Comment on the morphology of the red blood cells.
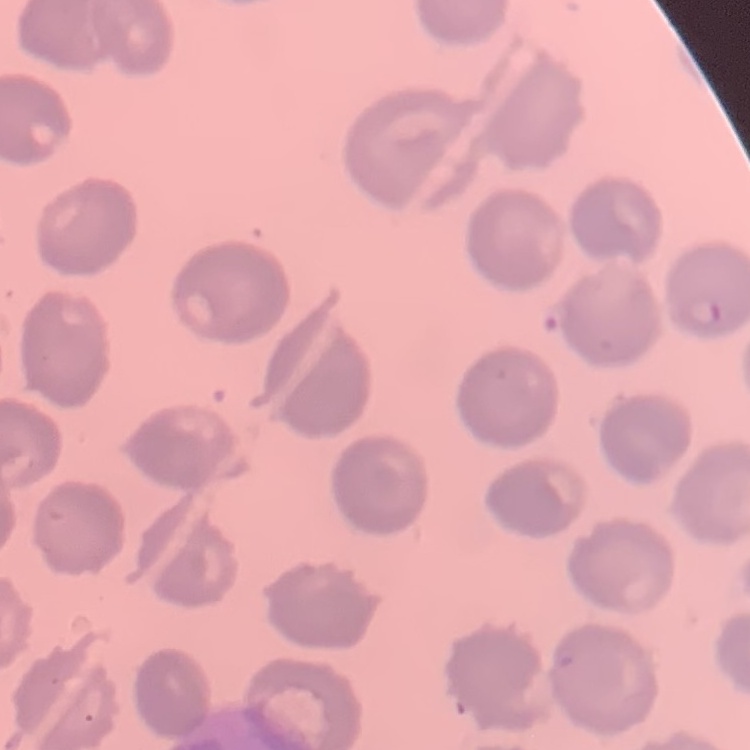
They show no rouleaux formation.

preparation = thin blood film
image type = one tile cut from a larger photomicrograph
stain = Field's or Giemsa